Describe the morphology of the erythrocytes.
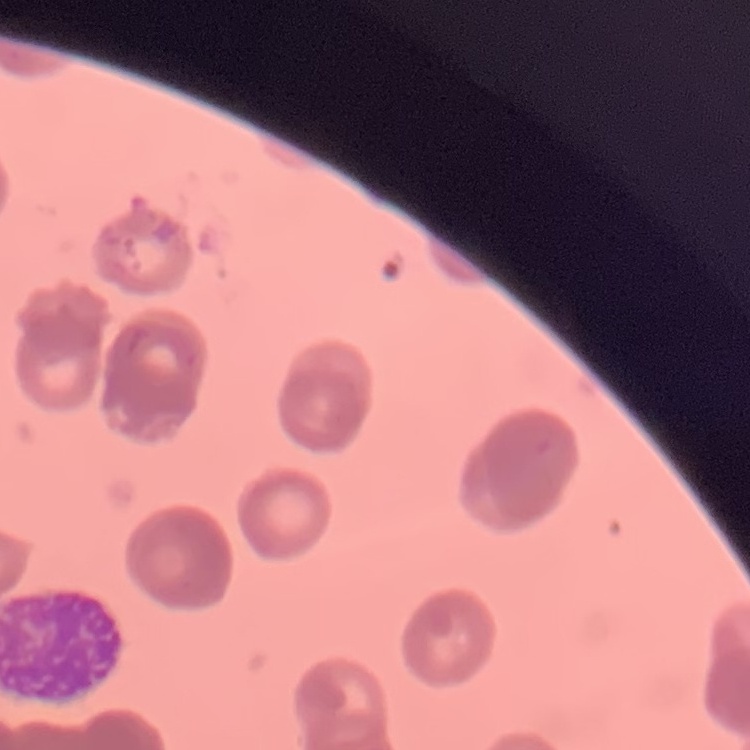

Rouleaux formation.

One tile cut from a larger photomicrograph. Stained with either Field's or Giemsa. Thin peripheral smear.